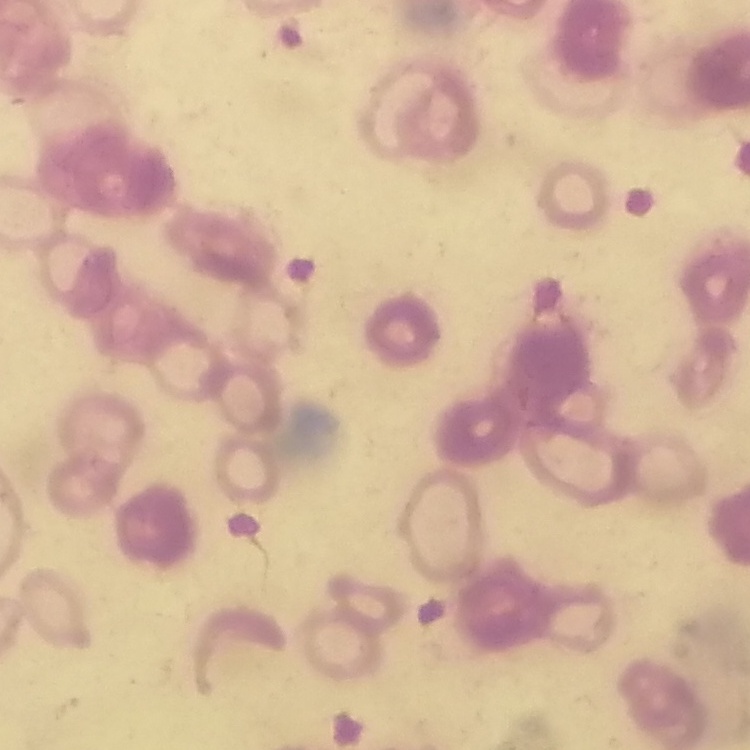
erythrocyte_morphology: rouleaux formation
preparation: thin peripheral smear
stain: Field's or Giemsa
image_type: one tile cut from a larger photomicrograph